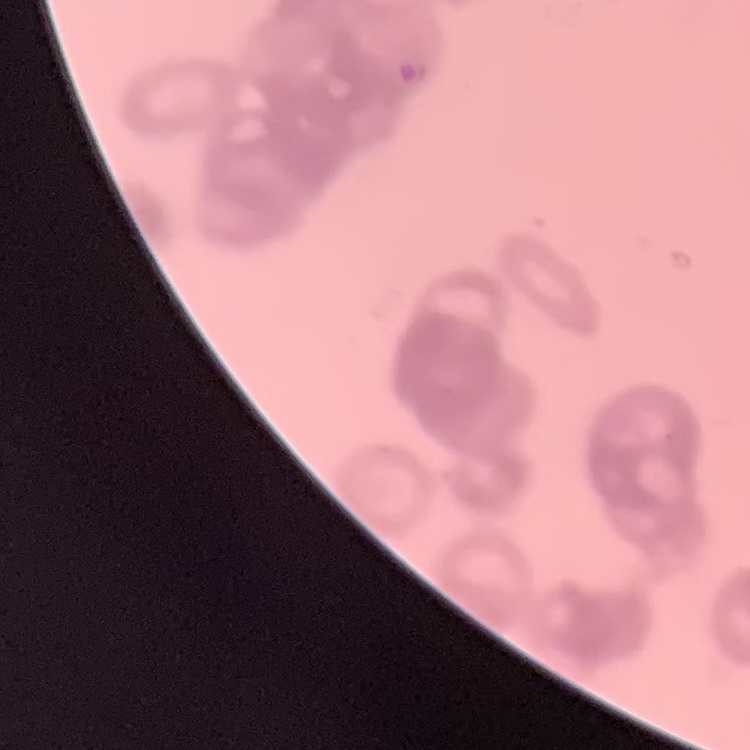

Summary:
  - Red blood cell morphology: rouleaux formation
  - Image type: square crop of a larger photomicrograph
  - Stain: Field's or Giemsa
  - Preparation: thin blood smear